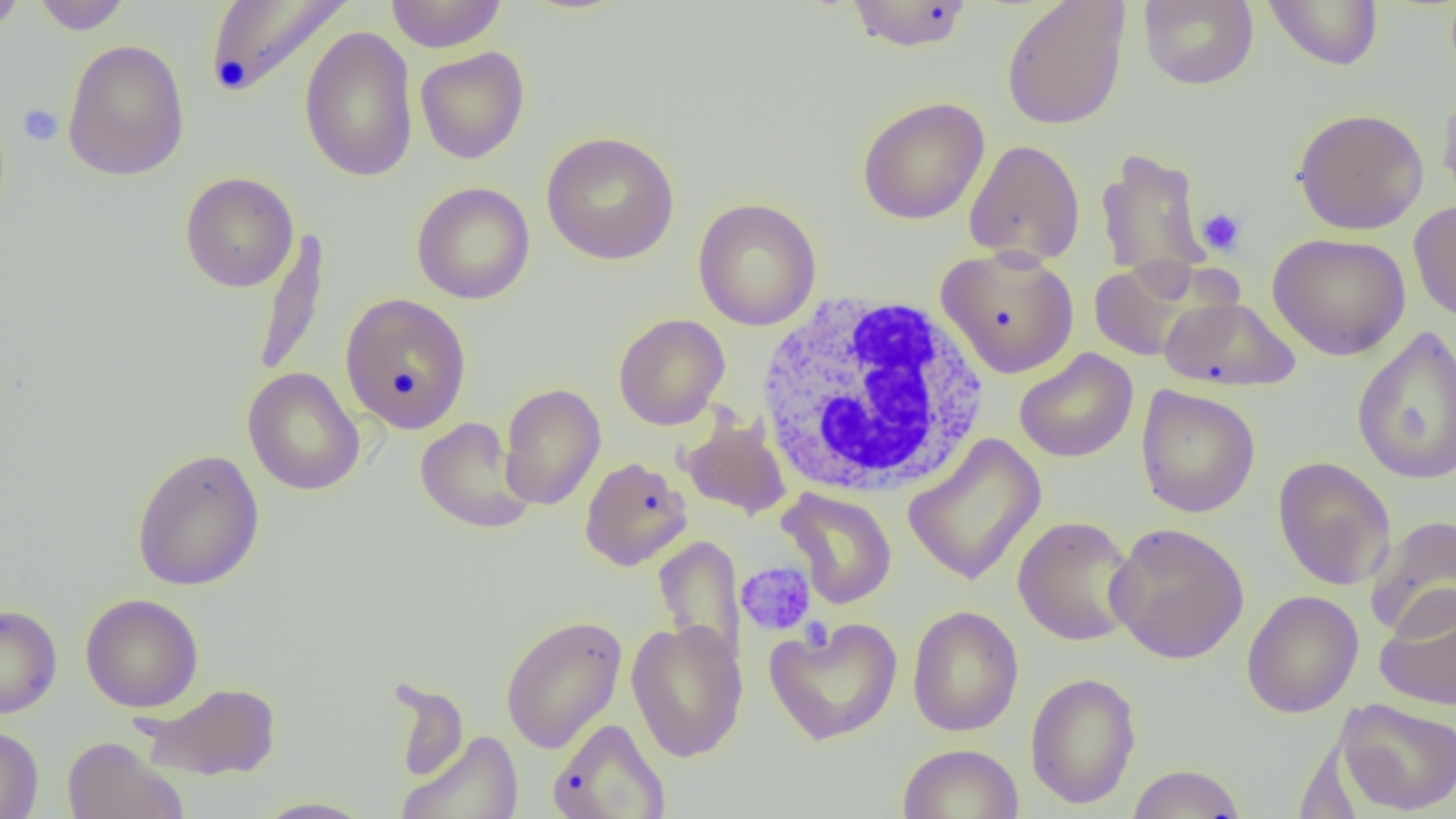

slide-level diagnosis = negative for blood parasites
platelet locations = approximate bounding boxes as named x1/y1/x2/y2 corners in pixels: (x1=18, y1=103, x2=63, y2=146), (x1=1197, y1=207, x2=1247, y2=257), (x1=736, y1=561, x2=817, y2=636), (x1=800, y1=617, x2=832, y2=650)
field of view = one of a larger specimen
image size = 1456×819 pixels
uninfected red blood cell locations = approximate bounding boxes as named x1/y1/x2/y2 corners in pixels: (x1=0, y1=0, x2=26, y2=34), (x1=31, y1=0, x2=133, y2=34), (x1=203, y1=0, x2=353, y2=100), (x1=385, y1=0, x2=507, y2=53), (x1=1139, y1=0, x2=1258, y2=90), (x1=1264, y1=0, x2=1384, y2=71), (x1=844, y1=1, x2=975, y2=52), (x1=1001, y1=1, x2=1131, y2=130), (x1=299, y1=25, x2=418, y2=184), (x1=62, y1=39, x2=190, y2=182), (x1=414, y1=46, x2=530, y2=164), (x1=1437, y1=86, x2=1456, y2=217), (x1=857, y1=97, x2=990, y2=225), (x1=1291, y1=108, x2=1429, y2=234), (x1=541, y1=131, x2=680, y2=265), (x1=963, y1=139, x2=1086, y2=267), (x1=1095, y1=145, x2=1212, y2=285), (x1=180, y1=172, x2=299, y2=293), (x1=412, y1=182, x2=535, y2=305), (x1=693, y1=197, x2=822, y2=331), (x1=1409, y1=200, x2=1456, y2=325), (x1=252, y1=228, x2=332, y2=380), (x1=1267, y1=232, x2=1411, y2=360), (x1=937, y1=247, x2=1079, y2=379), (x1=1088, y1=258, x2=1218, y2=362), (x1=340, y1=292, x2=472, y2=434), (x1=1159, y1=296, x2=1301, y2=392), (x1=613, y1=313, x2=729, y2=430), (x1=1351, y1=326, x2=1456, y2=485), (x1=1014, y1=348, x2=1138, y2=463), (x1=242, y1=367, x2=364, y2=496), (x1=499, y1=383, x2=606, y2=511), (x1=1135, y1=384, x2=1260, y2=518), (x1=415, y1=417, x2=535, y2=533), (x1=678, y1=417, x2=792, y2=520), (x1=903, y1=433, x2=1047, y2=587), (x1=131, y1=448, x2=265, y2=592), (x1=579, y1=456, x2=691, y2=571), (x1=1272, y1=456, x2=1396, y2=591), (x1=778, y1=488, x2=898, y2=609), (x1=1366, y1=514, x2=1456, y2=638), (x1=1012, y1=515, x2=1139, y2=646), (x1=1106, y1=522, x2=1250, y2=665), (x1=653, y1=534, x2=746, y2=669), (x1=1374, y1=588, x2=1456, y2=710), (x1=1241, y1=589, x2=1364, y2=718), (x1=80, y1=593, x2=203, y2=713), (x1=0, y1=604, x2=62, y2=718), (x1=907, y1=605, x2=1023, y2=737), (x1=501, y1=614, x2=627, y2=753), (x1=764, y1=617, x2=903, y2=746), (x1=627, y1=619, x2=748, y2=762), (x1=1025, y1=671, x2=1141, y2=810), (x1=388, y1=679, x2=469, y2=784), (x1=139, y1=681, x2=282, y2=781), (x1=1335, y1=698, x2=1456, y2=816), (x1=548, y1=717, x2=671, y2=819), (x1=0, y1=725, x2=43, y2=819), (x1=397, y1=731, x2=525, y2=819), (x1=62, y1=736, x2=188, y2=818), (x1=898, y1=743, x2=1023, y2=819), (x1=1125, y1=763, x2=1247, y2=818), (x1=252, y1=796, x2=378, y2=818)
white blood cell locations = approximate bounding boxes as named x1/y1/x2/y2 corners in pixels: (x1=755, y1=292, x2=991, y2=500)
magnification = 1000x
preparation = thin blood smear
modality = optical microscopy